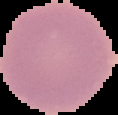

image size = 118×115 pixels
result = no Plasmodium parasites detected
preparation = thin blood smear
image type = cell region segmented out of the field of view; surrounding area masked to black